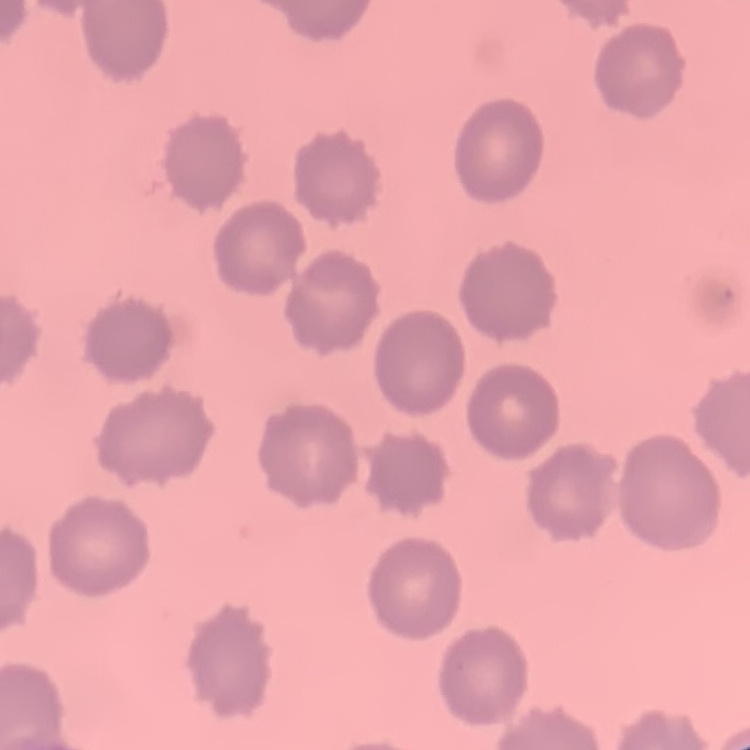

{
  "erythrocyte_morphology": "no rouleaux formation",
  "stain": "Field's or Giemsa",
  "image_type": "square crop of a larger photomicrograph",
  "preparation": "thin peripheral smear"
}